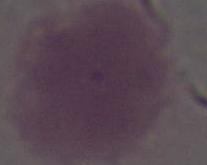 A red blood cell is shown. Photomicrograph. Captured at 1000x magnification.